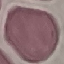
{
  "result": "no malaria parasites detected",
  "image_type": "automatically extracted cell patch, resized to 64 × 64 pixels",
  "preparation": "thin blood film",
  "capture": "smartphone through the microscope eyepiece",
  "stain": "Giemsa"
}